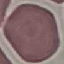
{
  "malaria_status": "uninfected",
  "image_type": "cell patch, automatically extracted from a larger field of view and resized to 64 × 64 pixels",
  "stain": "Giemsa",
  "capture": "smartphone through the microscope eyepiece",
  "preparation": "thin smear"
}